Assess this cell for malaria.
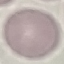

Uninfected.

Giemsa-stained preparation. Thin blood smear. Photographed with a smartphone camera at the microscope eyepiece. Automatically extracted cell patch, resized to 64 × 64 pixels.